Locate every blood parasite and identify its species.
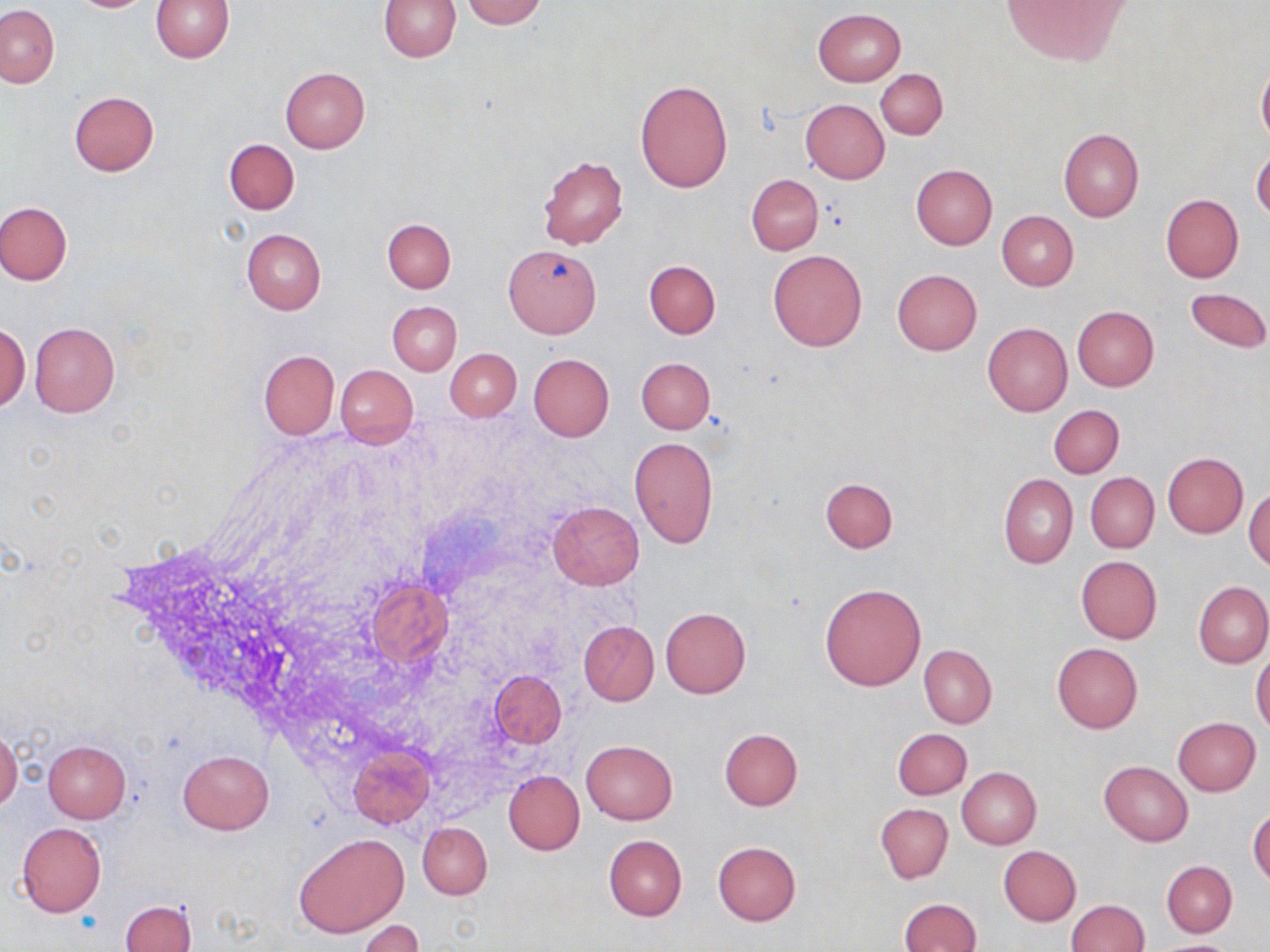
No blood parasites observed.

Approximate bounding boxes as [x1, y1, x2, y2] in pixels. Uninfected red blood cell locations: [69, 0, 159, 13], [150, 0, 234, 62], [379, 0, 461, 62], [463, 0, 545, 28], [999, 0, 1133, 65], [0, 5, 58, 87], [813, 8, 905, 86], [1256, 62, 1270, 147], [279, 67, 369, 153], [875, 69, 948, 140], [635, 78, 733, 193], [69, 90, 159, 175], [801, 99, 889, 183], [1057, 127, 1143, 222], [224, 138, 298, 215], [1252, 149, 1270, 220], [538, 155, 628, 251], [911, 164, 997, 249], [746, 174, 823, 255], [1161, 194, 1243, 284], [0, 202, 72, 285], [996, 210, 1078, 290], [383, 218, 455, 293], [241, 228, 325, 314], [504, 245, 602, 337], [768, 249, 867, 351], [644, 259, 720, 338], [891, 269, 983, 355], [1183, 287, 1270, 354], [387, 301, 461, 375], [1072, 305, 1158, 390], [28, 322, 120, 417], [983, 322, 1072, 416], [0, 323, 30, 413], [445, 348, 521, 421], [258, 350, 339, 439], [528, 353, 614, 441], [636, 357, 715, 434], [336, 365, 417, 447], [1049, 405, 1123, 477], [628, 436, 717, 550], [1163, 453, 1247, 538], [1085, 472, 1158, 553], [999, 474, 1078, 569], [821, 477, 898, 553], [1245, 488, 1270, 571], [547, 501, 644, 589], [1076, 556, 1162, 644], [364, 579, 453, 669], [1194, 582, 1270, 667], [821, 584, 925, 690], [660, 606, 750, 698], [579, 620, 659, 706], [1052, 643, 1143, 733], [919, 645, 996, 727], [1252, 652, 1270, 734], [490, 670, 566, 749], [1172, 717, 1261, 795], [893, 728, 971, 799], [719, 729, 803, 811], [0, 731, 22, 813], [581, 739, 677, 825], [41, 740, 131, 823], [349, 747, 434, 827], [178, 749, 274, 833], [1099, 761, 1193, 846], [957, 767, 1042, 849], [504, 770, 584, 855], [876, 803, 952, 883], [1248, 807, 1270, 888], [16, 822, 106, 916], [417, 822, 492, 899], [294, 834, 408, 937], [604, 834, 687, 920], [713, 842, 801, 926], [998, 846, 1081, 925], [1162, 860, 1237, 937], [898, 898, 981, 952], [120, 899, 197, 952], [1066, 900, 1148, 952], [359, 920, 423, 952], [1151, 939, 1239, 952]. Slide-level diagnosis: no evidence of blood parasites. May-Grünwald-Giemsa stain. Single field of view. Light microscopy. Thin blood smear. Image is 1270×952 pixels. 1000x magnification.